Classify this cell by malaria status.
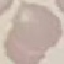
Uninfected.

stain = Giemsa
image type = cell patch, automatically extracted from a larger field of view and resized to 64 × 64 pixels
capture = smartphone through the microscope eyepiece
preparation = thin blood smear